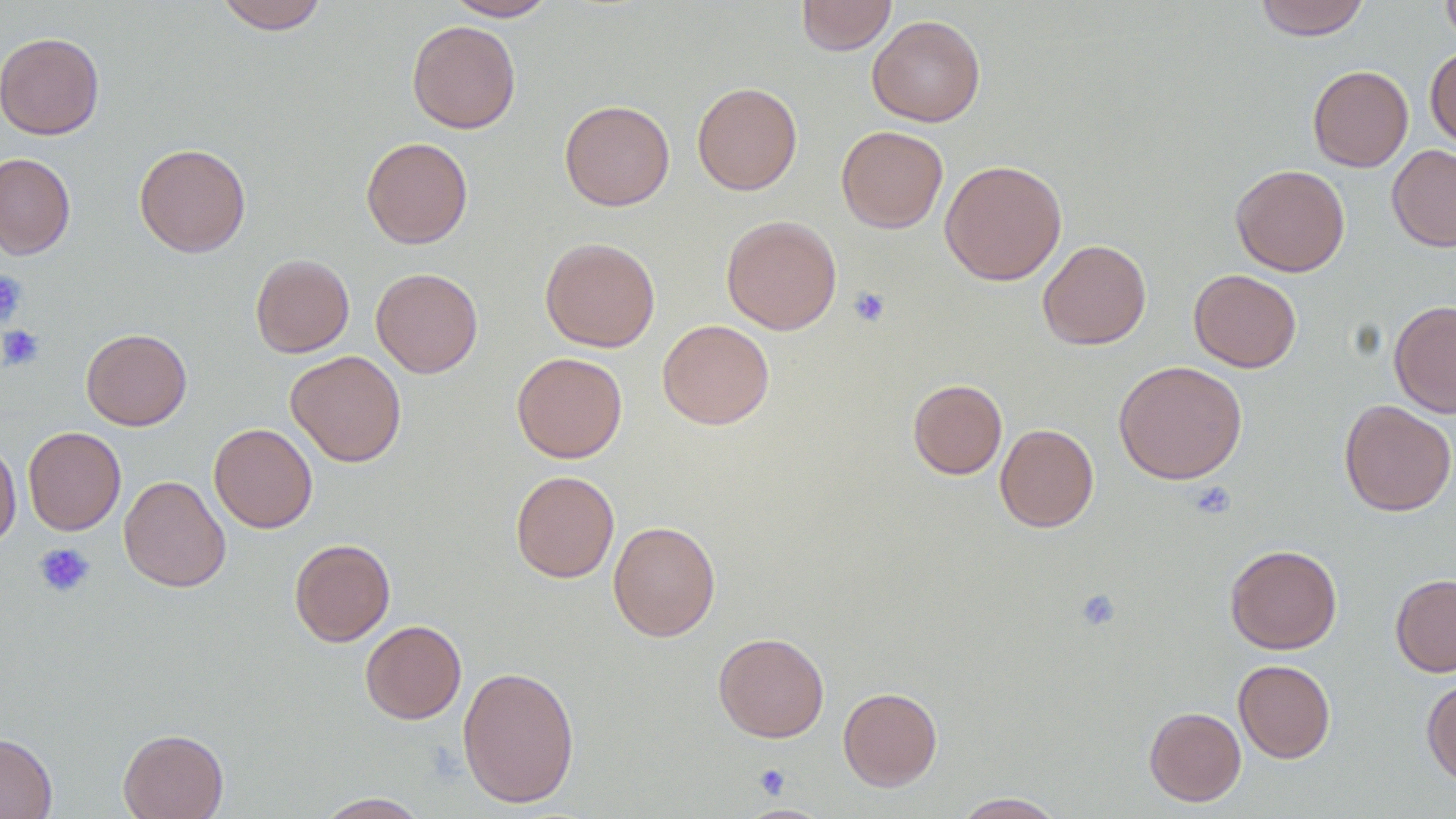

Summary:
  - Coordinate format: approximate bounding boxes as (x1,y1)-(x2,y2) corner pairs in pixels
  - Platelet locations: (0,272)-(27,326), (848,287)-(891,327), (0,324)-(45,371), (1188,480)-(1236,520), (33,543)-(95,598), (1074,587)-(1121,631), (753,763)-(790,799)
  - Uninfected red blood cell locations: (215,0)-(329,34), (443,0)-(557,21), (796,0)-(897,55), (1254,0)-(1369,40), (1441,0)-(1456,49), (867,15)-(985,126), (407,20)-(521,134), (0,32)-(105,140), (1425,45)-(1456,149), (1308,65)-(1413,172), (691,81)-(803,195), (560,99)-(675,210), (836,125)-(948,233), (360,137)-(473,249), (134,142)-(251,257), (1387,144)-(1456,252), (0,153)-(76,259), (940,159)-(1067,286), (1231,164)-(1349,276), (721,215)-(842,334), (540,236)-(660,352), (1038,239)-(1151,350), (250,253)-(355,358), (371,267)-(483,378), (1189,269)-(1302,372), (1389,299)-(1456,419), (657,319)-(774,430), (81,328)-(192,430), (286,350)-(406,467), (512,352)-(627,463), (1114,360)-(1248,484), (908,378)-(1007,480), (1339,399)-(1456,516), (209,423)-(318,533), (995,424)-(1099,532), (23,427)-(126,535), (0,439)-(21,548), (510,470)-(619,583), (119,475)-(231,592), (608,520)-(720,642), (289,538)-(395,646), (1225,544)-(1342,654), (1390,574)-(1456,676), (360,620)-(466,724), (713,631)-(829,742), (1233,659)-(1336,763), (457,665)-(580,808), (1422,677)-(1456,787), (838,686)-(942,791), (1144,706)-(1246,806), (118,728)-(229,819), (0,732)-(57,819), (313,792)-(431,818), (951,792)-(1066,818), (736,803)-(835,818)
  - Slide-level diagnosis: no evidence of blood parasites
  - Field of view: one of a larger specimen
  - Magnification: 1000x
  - Modality: light microscopy
  - Preparation: thin blood smear
  - Image size: 1456×819 pixels